Identify the parasite.
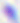

This is Toxoplasma gondii.

{
  "modality": "photomicrograph",
  "magnification": "400x"
}